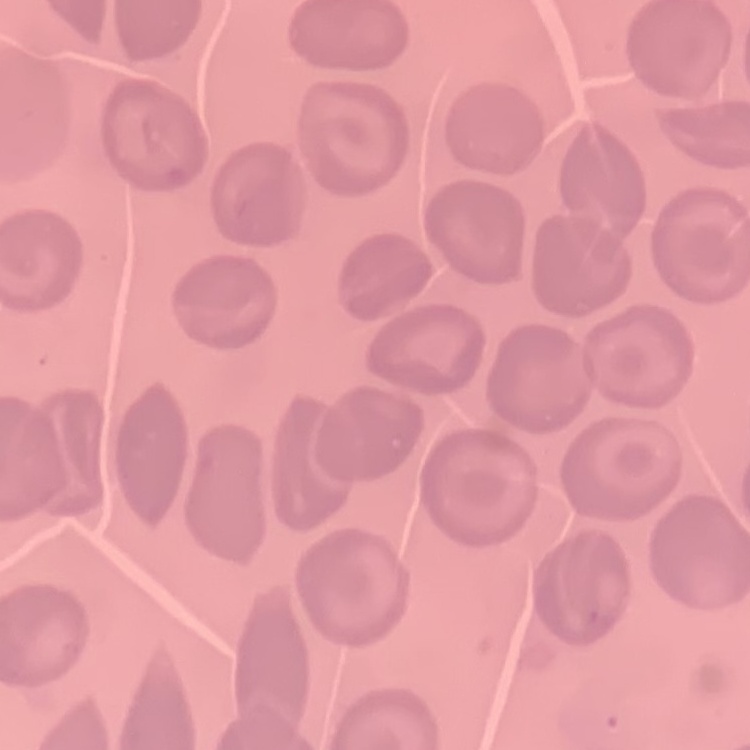
The erythrocytes exhibit no rouleaux formation. Square crop of a larger photomicrograph. Stained with either Field's or Giemsa. Thin blood smear.